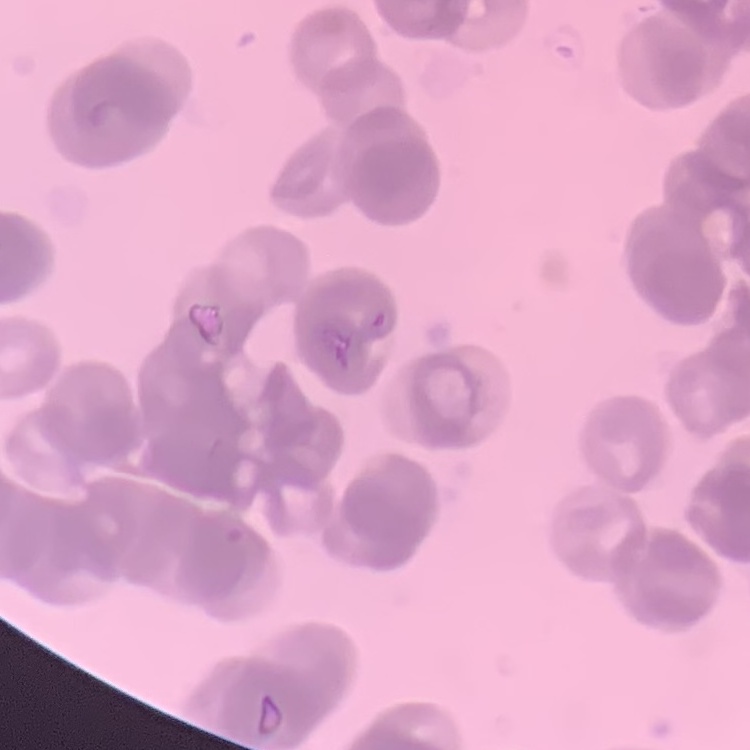

Summary:
  - Red blood cell morphology: rouleaux formation
  - Preparation: thin peripheral smear
  - Stain: Field's or Giemsa
  - Image type: one tile cut from a larger photomicrograph